Point out each malaria parasite and each leukocyte.
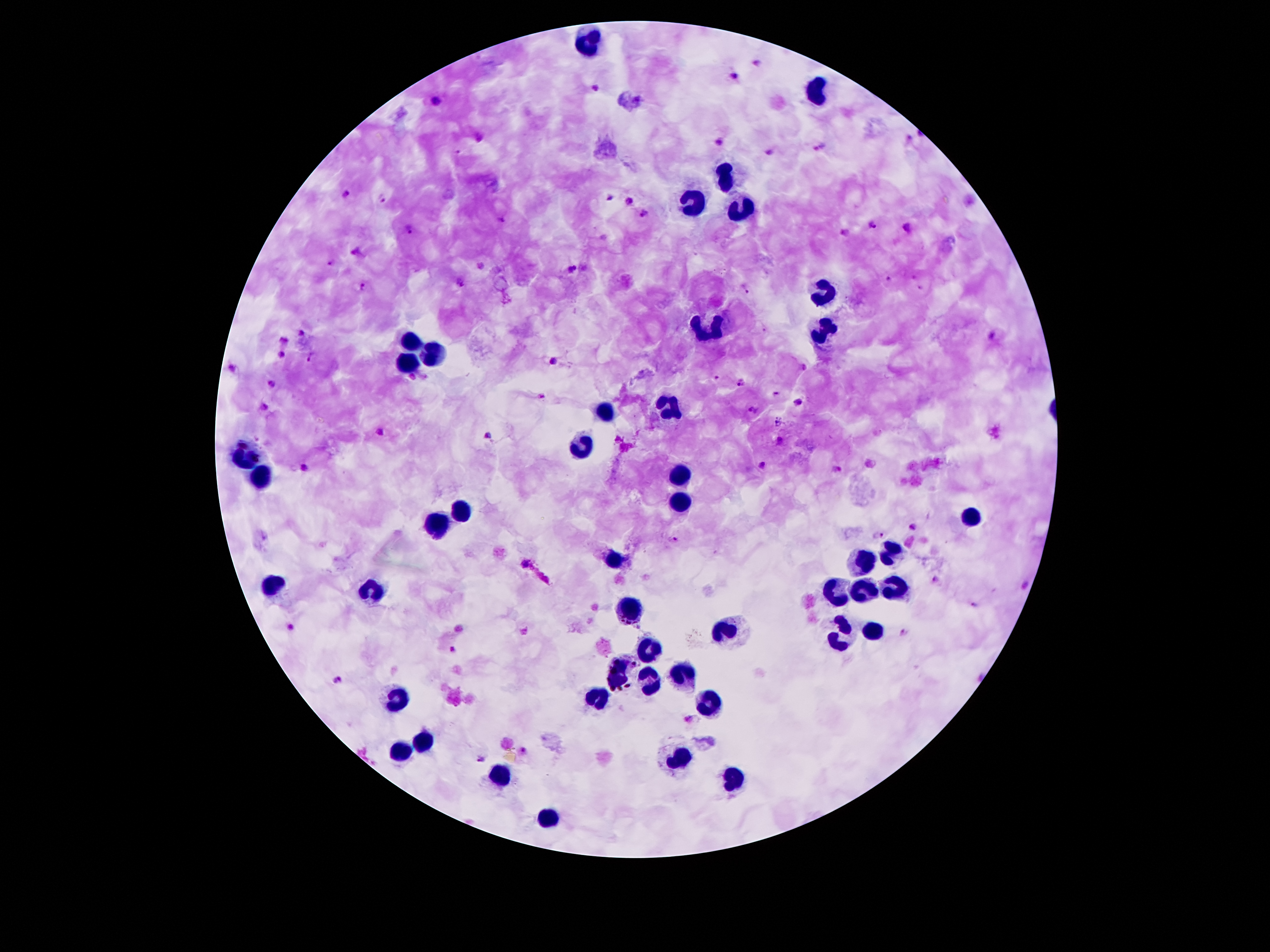
Approximate centers as [x, y] in pixels.
Malaria parasites: [756, 64], [735, 76], [595, 87], [438, 101], [480, 136], [910, 138], [720, 141], [821, 148], [457, 151], [770, 151], [347, 193], [609, 196], [382, 197], [629, 202], [645, 215], [503, 219], [873, 224], [910, 225], [409, 229], [845, 233], [358, 250], [331, 262], [572, 268], [913, 277], [889, 279], [460, 281], [362, 287], [921, 287], [746, 289], [300, 332], [991, 337], [283, 339], [282, 355], [310, 357], [555, 360], [233, 367], [717, 376], [741, 381], [273, 384], [776, 394], [540, 395], [799, 401], [264, 406], [753, 409], [778, 424], [379, 432], [487, 436], [781, 441], [765, 465], [304, 467], [837, 470], [912, 525], [880, 536], [675, 538], [527, 564], [936, 579], [1026, 584], [975, 605], [290, 625], [904, 632], [453, 648], [338, 678], [687, 718], [524, 751], [481, 758].
Leukocytes: [588, 39], [814, 93], [725, 178], [695, 205], [738, 210], [822, 291], [709, 329], [825, 333], [411, 339], [432, 353], [408, 360], [667, 407], [609, 411], [583, 446], [247, 453], [262, 474], [681, 476], [677, 505], [462, 509], [971, 518], [436, 526], [892, 549], [614, 558], [864, 563], [275, 584], [894, 588], [374, 589], [861, 589], [840, 595], [628, 609], [875, 631], [728, 635], [842, 635], [649, 652], [619, 672], [688, 677], [647, 684], [595, 698], [401, 701], [712, 705], [418, 740], [401, 752], [677, 756], [504, 773], [731, 776], [546, 818].

capture = smartphone through the microscope eyepiece
patient malaria status = positive for Plasmodium falciparum
preparation = thick peripheral-blood smear
field of view = one from this slide
stain = Giemsa
image size = 1270×952 pixels
magnification = 100x